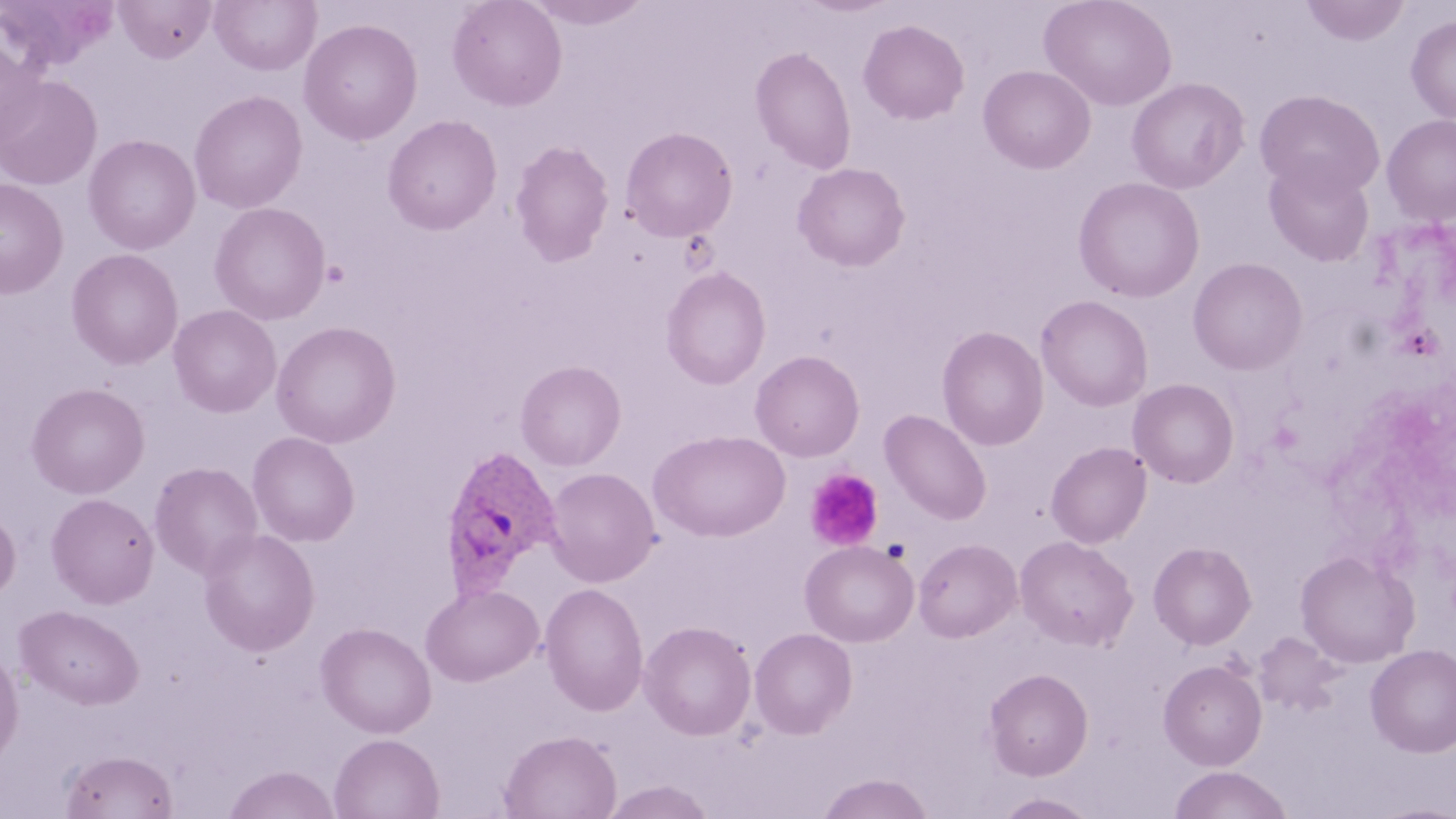

Approximate bounding boxes as named x1/y1/x2/y2 corners in pixels. Plasmodium ovale-infected red blood cell locations: (x1=438, y1=444, x2=563, y2=598). Uninfected red blood cell locations: (x1=114, y1=0, x2=216, y2=62), (x1=209, y1=0, x2=321, y2=76), (x1=447, y1=0, x2=567, y2=112), (x1=527, y1=0, x2=652, y2=29), (x1=796, y1=0, x2=898, y2=17), (x1=1040, y1=0, x2=1177, y2=111), (x1=1301, y1=0, x2=1409, y2=46), (x1=1, y1=1, x2=118, y2=73), (x1=1405, y1=16, x2=1456, y2=123), (x1=299, y1=18, x2=423, y2=145), (x1=858, y1=19, x2=970, y2=125), (x1=0, y1=38, x2=44, y2=150), (x1=750, y1=46, x2=857, y2=174), (x1=978, y1=65, x2=1096, y2=174), (x1=0, y1=74, x2=102, y2=189), (x1=1127, y1=77, x2=1249, y2=194), (x1=1255, y1=89, x2=1385, y2=198), (x1=189, y1=90, x2=307, y2=213), (x1=1382, y1=114, x2=1456, y2=225), (x1=382, y1=115, x2=503, y2=236), (x1=621, y1=126, x2=738, y2=242), (x1=82, y1=133, x2=201, y2=255), (x1=509, y1=140, x2=614, y2=266), (x1=1264, y1=157, x2=1375, y2=266), (x1=793, y1=162, x2=910, y2=271), (x1=1073, y1=176, x2=1205, y2=303), (x1=0, y1=177, x2=68, y2=299), (x1=209, y1=202, x2=331, y2=325), (x1=66, y1=248, x2=184, y2=370), (x1=1188, y1=257, x2=1308, y2=375), (x1=661, y1=266, x2=771, y2=390), (x1=1036, y1=295, x2=1153, y2=411), (x1=168, y1=304, x2=281, y2=418), (x1=271, y1=321, x2=401, y2=449), (x1=936, y1=326, x2=1049, y2=451), (x1=750, y1=350, x2=865, y2=462), (x1=515, y1=361, x2=626, y2=470), (x1=1128, y1=378, x2=1239, y2=488), (x1=26, y1=382, x2=150, y2=499), (x1=880, y1=409, x2=992, y2=525), (x1=649, y1=430, x2=790, y2=542), (x1=247, y1=431, x2=360, y2=547), (x1=1046, y1=441, x2=1151, y2=548), (x1=149, y1=461, x2=263, y2=579), (x1=544, y1=466, x2=661, y2=587), (x1=46, y1=492, x2=160, y2=609), (x1=0, y1=507, x2=21, y2=603), (x1=197, y1=528, x2=320, y2=656), (x1=1015, y1=535, x2=1138, y2=651), (x1=913, y1=538, x2=1021, y2=642), (x1=800, y1=540, x2=919, y2=647), (x1=1155, y1=541, x2=1261, y2=769), (x1=1149, y1=542, x2=1256, y2=650), (x1=1296, y1=550, x2=1419, y2=668), (x1=539, y1=583, x2=649, y2=716), (x1=420, y1=584, x2=544, y2=687), (x1=15, y1=605, x2=143, y2=709), (x1=639, y1=621, x2=757, y2=740), (x1=316, y1=622, x2=436, y2=738), (x1=750, y1=627, x2=857, y2=738), (x1=1253, y1=632, x2=1344, y2=716), (x1=1366, y1=644, x2=1456, y2=758), (x1=0, y1=649, x2=24, y2=765), (x1=1159, y1=660, x2=1267, y2=770), (x1=984, y1=668, x2=1094, y2=780), (x1=498, y1=730, x2=621, y2=818), (x1=329, y1=733, x2=444, y2=819), (x1=60, y1=749, x2=178, y2=818), (x1=224, y1=765, x2=340, y2=819), (x1=1169, y1=765, x2=1294, y2=819), (x1=816, y1=773, x2=934, y2=819), (x1=602, y1=781, x2=717, y2=819), (x1=993, y1=792, x2=1101, y2=819). Platelet locations: (x1=805, y1=468, x2=885, y2=552). Slide-level diagnosis: Plasmodium ovale. Light microscopy. 1000x magnification. Image is 1456×819 pixels. Thin blood film. May-Grünwald-Giemsa-stained preparation. Single field of view.